Describe the morphology of the erythrocytes.
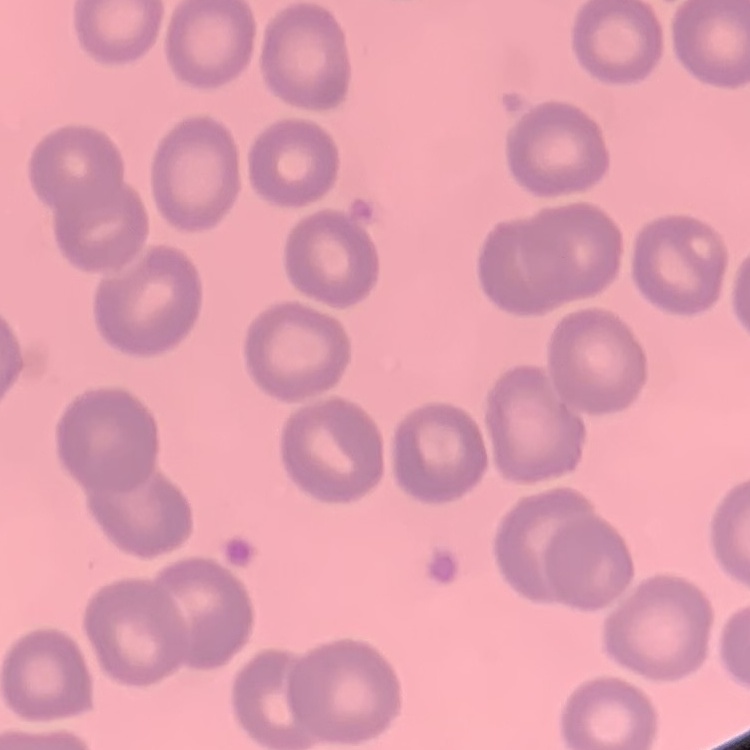

They show no rouleaux formation.

Summary:
  - Preparation: thin blood smear
  - Image type: square crop of a larger photomicrograph
  - Stain: Field's or Giemsa